Assess this cell for malaria.
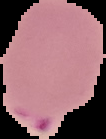
Parasitized.

The area outside the segmented cell region is set to black. Image is 106×139 pixels. From a thin blood film.